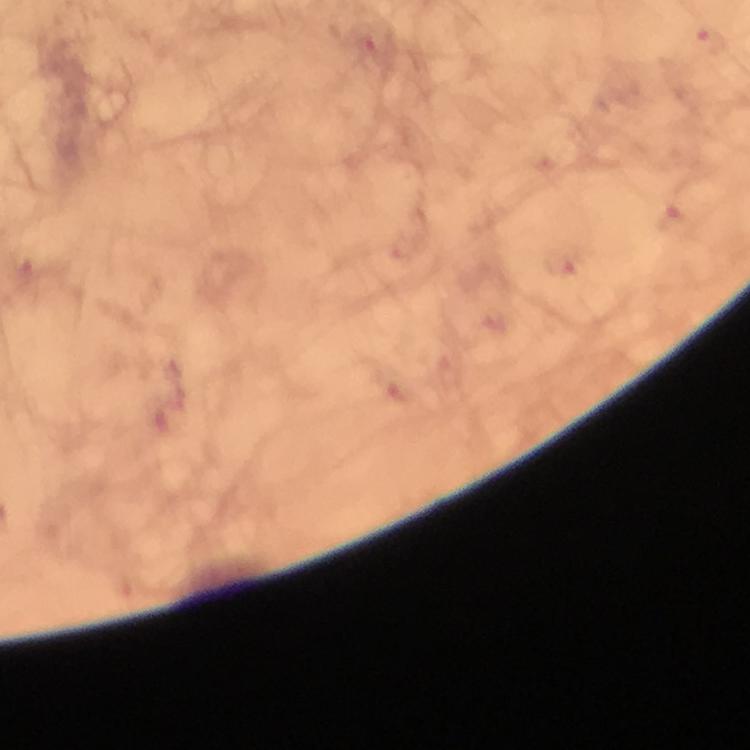
{
  "cropped_from": "one field of view",
  "malaria_parasite_locations": "approximate centers as [x, y] in pixels: [364, 41], [711, 42], [674, 218], [559, 265]",
  "context": "from a diagnostic examination for malaria",
  "image_size": "750×750 pixels",
  "magnification": "100x",
  "immersion_oil": "applied",
  "preparation": "thick smear",
  "capture": "smartphone camera through the microscope",
  "stain": "Giemsa"
}